Identify the parasite.
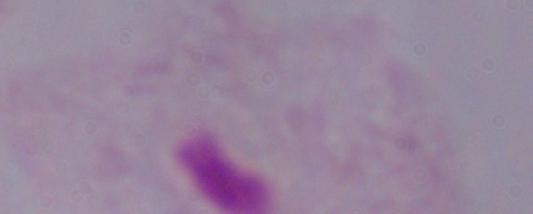
A trichomonad.

Summary:
  - Magnification: 1000x
  - Modality: photomicrograph